Assess this cell for malaria.
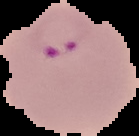
It is parasitized.

The area outside the segmented cell region is set to black. Image is 139×136 pixels. From a thin blood film.